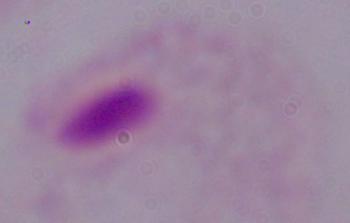
Captured at 1000x magnification. A trichomonad is seen. Photomicrograph.